Identify the cell.
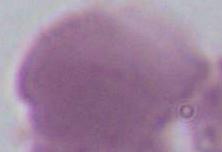

An erythrocyte.

magnification = 1000x
modality = photomicrograph